Locate and identify every blood parasite.
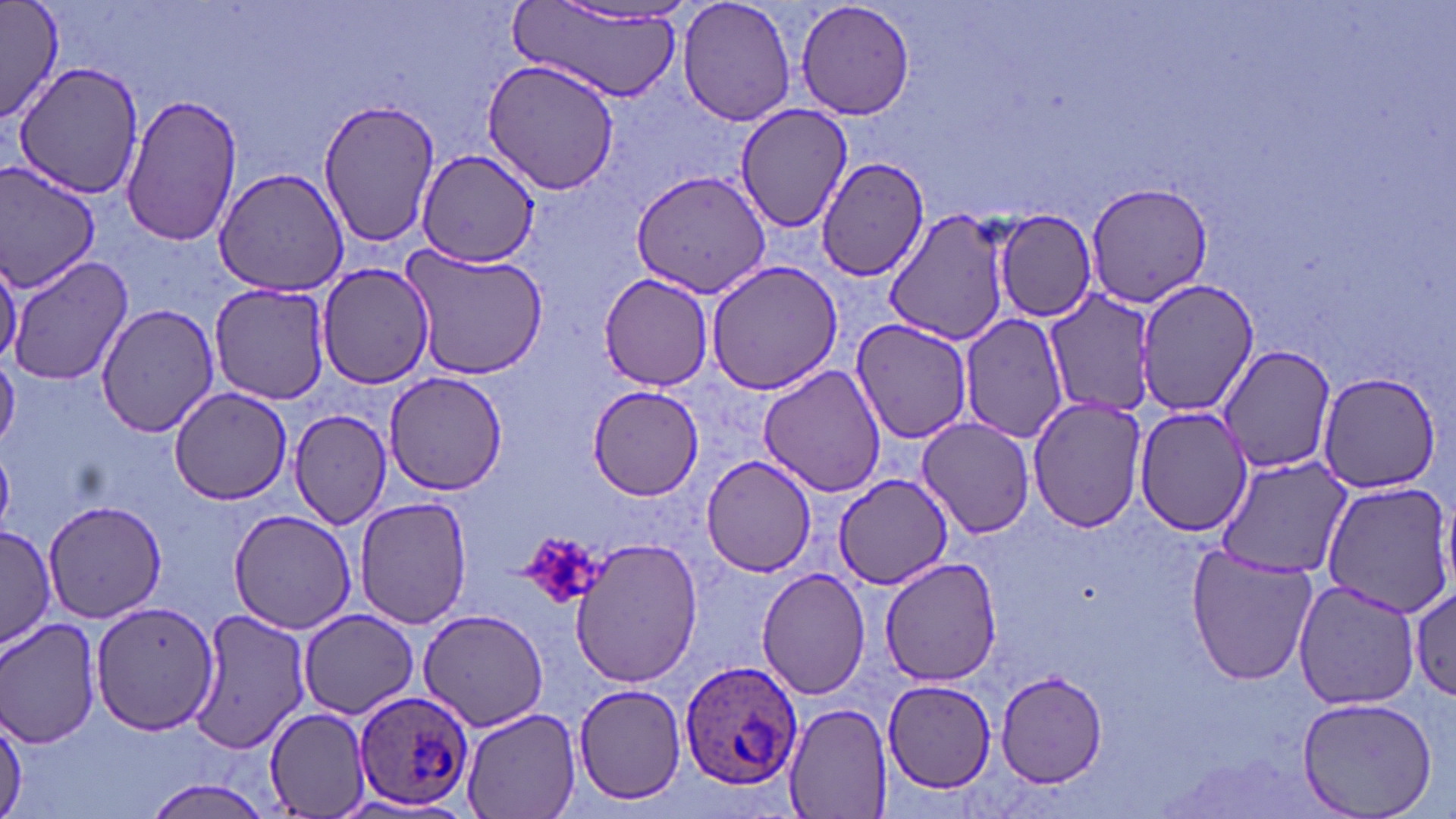

Approximate bounding boxes as named x1/y1/x2/y2 corners in pixels.
Plasmodium ovale-infected red blood cells: (x1=676, y1=659, x2=802, y2=792), (x1=353, y1=690, x2=476, y2=810).
No Plasmodium falciparum, Plasmodium malariae, Plasmodium vivax, Babesia divergens, or Trypanosoma brucei observed.

Uninfected red blood cell locations: (x1=1, y1=0, x2=62, y2=122), (x1=677, y1=0, x2=798, y2=127), (x1=795, y1=0, x2=916, y2=121), (x1=509, y1=3, x2=686, y2=103), (x1=481, y1=57, x2=623, y2=196), (x1=12, y1=63, x2=143, y2=198), (x1=120, y1=92, x2=243, y2=246), (x1=313, y1=100, x2=441, y2=250), (x1=735, y1=103, x2=854, y2=233), (x1=414, y1=149, x2=540, y2=267), (x1=815, y1=156, x2=928, y2=282), (x1=0, y1=164, x2=99, y2=293), (x1=214, y1=168, x2=351, y2=298), (x1=632, y1=169, x2=773, y2=299), (x1=1085, y1=181, x2=1212, y2=309), (x1=882, y1=205, x2=1012, y2=348), (x1=992, y1=208, x2=1098, y2=323), (x1=401, y1=243, x2=549, y2=380), (x1=0, y1=253, x2=21, y2=367), (x1=7, y1=254, x2=133, y2=387), (x1=704, y1=259, x2=845, y2=396), (x1=317, y1=262, x2=434, y2=390), (x1=599, y1=273, x2=714, y2=389), (x1=1136, y1=277, x2=1256, y2=417), (x1=209, y1=283, x2=333, y2=404), (x1=1046, y1=287, x2=1164, y2=416), (x1=97, y1=302, x2=221, y2=436), (x1=960, y1=313, x2=1070, y2=444), (x1=851, y1=318, x2=975, y2=445), (x1=1217, y1=342, x2=1338, y2=473), (x1=0, y1=350, x2=20, y2=451), (x1=758, y1=362, x2=886, y2=498), (x1=384, y1=371, x2=508, y2=495), (x1=1315, y1=373, x2=1442, y2=494), (x1=587, y1=384, x2=704, y2=499), (x1=169, y1=387, x2=293, y2=505), (x1=1027, y1=394, x2=1148, y2=533), (x1=1134, y1=406, x2=1252, y2=537), (x1=290, y1=408, x2=392, y2=529), (x1=916, y1=416, x2=1035, y2=537), (x1=700, y1=455, x2=817, y2=576), (x1=1213, y1=456, x2=1354, y2=579), (x1=833, y1=471, x2=953, y2=591), (x1=1320, y1=481, x2=1456, y2=618), (x1=354, y1=496, x2=472, y2=629), (x1=43, y1=499, x2=166, y2=623), (x1=228, y1=507, x2=357, y2=633), (x1=1, y1=522, x2=56, y2=653), (x1=569, y1=537, x2=703, y2=690), (x1=1185, y1=545, x2=1318, y2=686), (x1=880, y1=559, x2=1003, y2=685), (x1=756, y1=567, x2=871, y2=699), (x1=1293, y1=579, x2=1424, y2=711), (x1=1410, y1=580, x2=1454, y2=704), (x1=91, y1=599, x2=222, y2=734), (x1=417, y1=607, x2=551, y2=733), (x1=187, y1=608, x2=309, y2=755), (x1=297, y1=609, x2=418, y2=717), (x1=1, y1=616, x2=102, y2=749), (x1=995, y1=673, x2=1108, y2=788), (x1=882, y1=679, x2=995, y2=792), (x1=573, y1=681, x2=689, y2=806), (x1=1298, y1=696, x2=1440, y2=818), (x1=783, y1=701, x2=893, y2=819), (x1=263, y1=705, x2=372, y2=816), (x1=460, y1=707, x2=580, y2=819), (x1=1, y1=709, x2=26, y2=817). Platelet locations: (x1=522, y1=531, x2=604, y2=611). Slide-level diagnosis: Plasmodium ovale. Single field of view. Thin blood smear. Image is 1456×819 pixels. May-Grünwald-Giemsa stain. 1000x magnification. Light microscopy.